Comment on the morphology of the red blood cells.
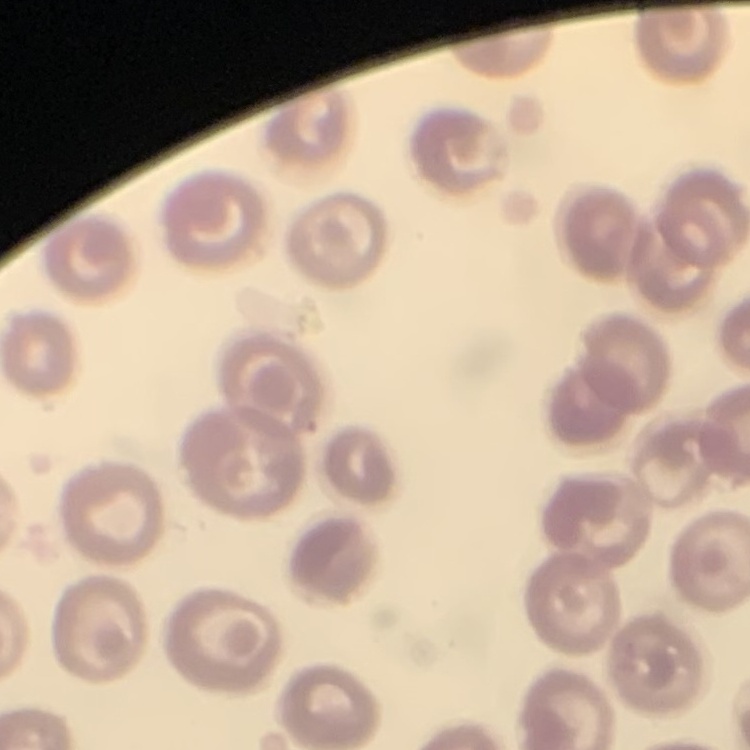
No rouleaux formation.

preparation = thin peripheral smear
image type = square crop of a larger photomicrograph
stain = Field's or Giemsa